Name the parasite shown.
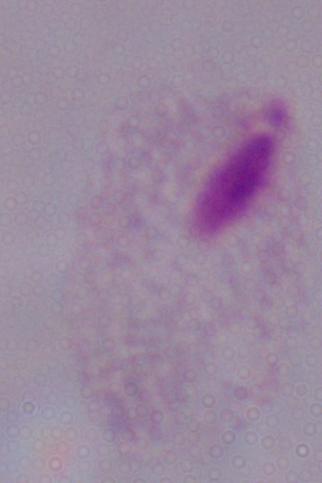
This is a trichomonad.

Summary:
  - Magnification: 1000x
  - Modality: micrograph